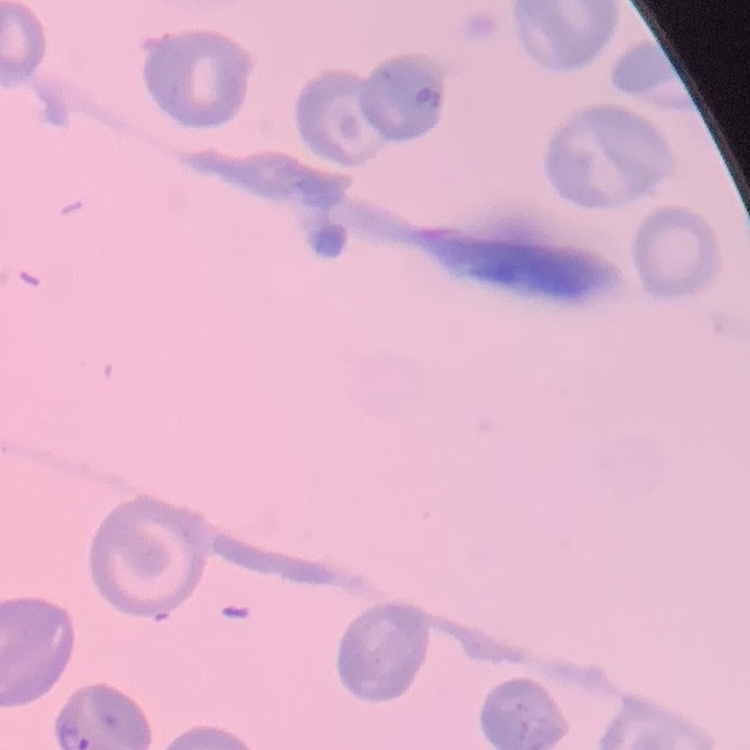

The erythrocytes exhibit no rouleaux formation. Thin blood smear. Field's or Giemsa stain. Square crop of a larger photomicrograph.